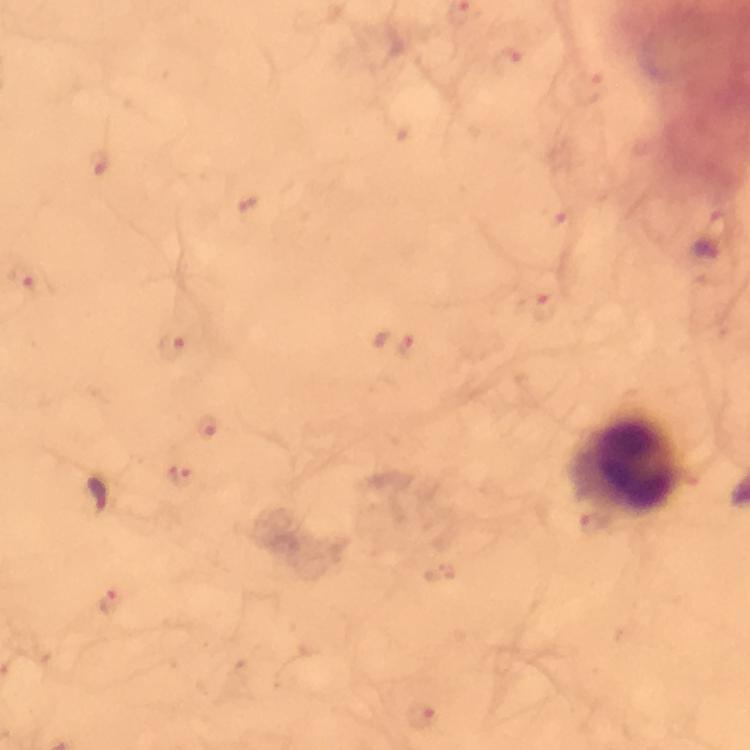 Approximate object centers, in pixels from the top-left corner. Leukocyte locations: (x=630, y=465). Malaria parasite locations: (x=507, y=62), (x=98, y=162), (x=23, y=276), (x=393, y=343), (x=174, y=346), (x=181, y=476), (x=95, y=496), (x=422, y=715). Image is 750×750 pixels. Giemsa stain. At 100x magnification. Thick blood smear. Immersion oil was used. A crop from one field of view. From a diagnostic examination for malaria. Photographed through the microscope with a smartphone camera.